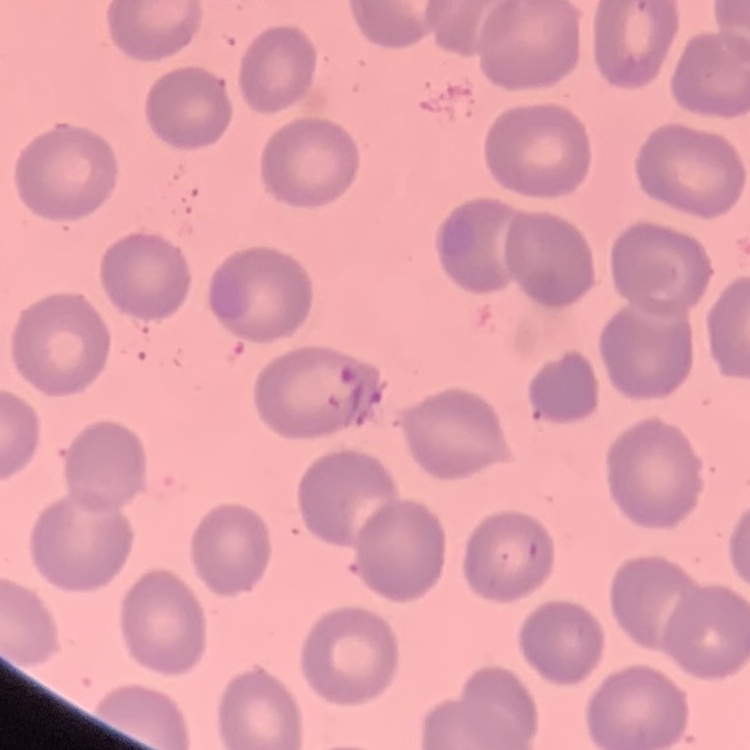
{
  "erythrocyte_morphology": "no rouleaux formation",
  "preparation": "thin blood film",
  "image_type": "one tile cut from a larger photomicrograph",
  "stain": "Field's or Giemsa"
}